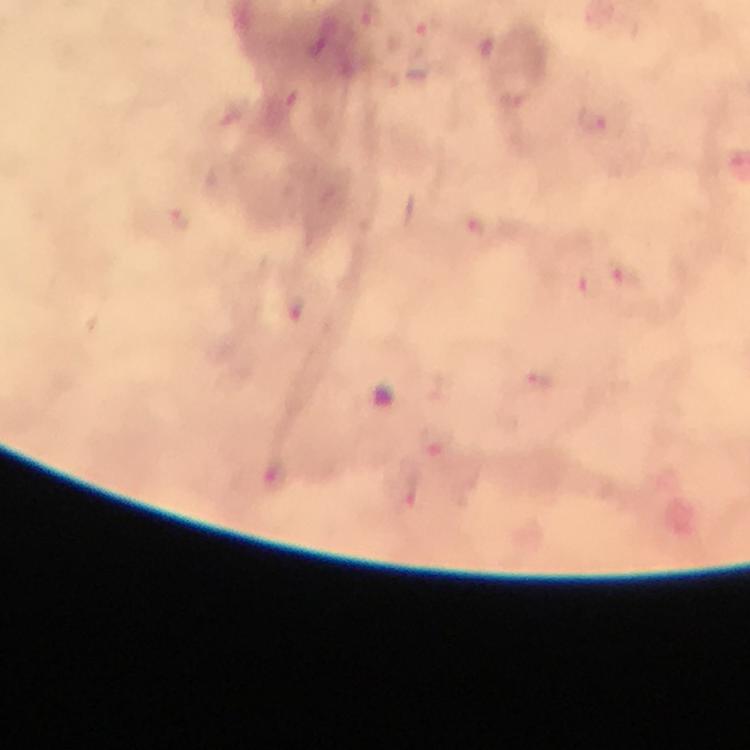
{
  "image_size": "750×750 pixels",
  "context": "from a malaria diagnostic workup",
  "malaria_parasite_locations": "approximate centers as [x, y] in pixels: [427, 30], [288, 98], [591, 119], [180, 220], [477, 228], [626, 275], [588, 283], [542, 382], [436, 442]",
  "preparation": "thick blood film",
  "stain": "Giemsa",
  "capture": "smartphone photograph through a microscope",
  "cropped_from": "a single field of view",
  "magnification": "100x",
  "immersion_oil": "applied"
}